Describe the morphology of the erythrocytes.
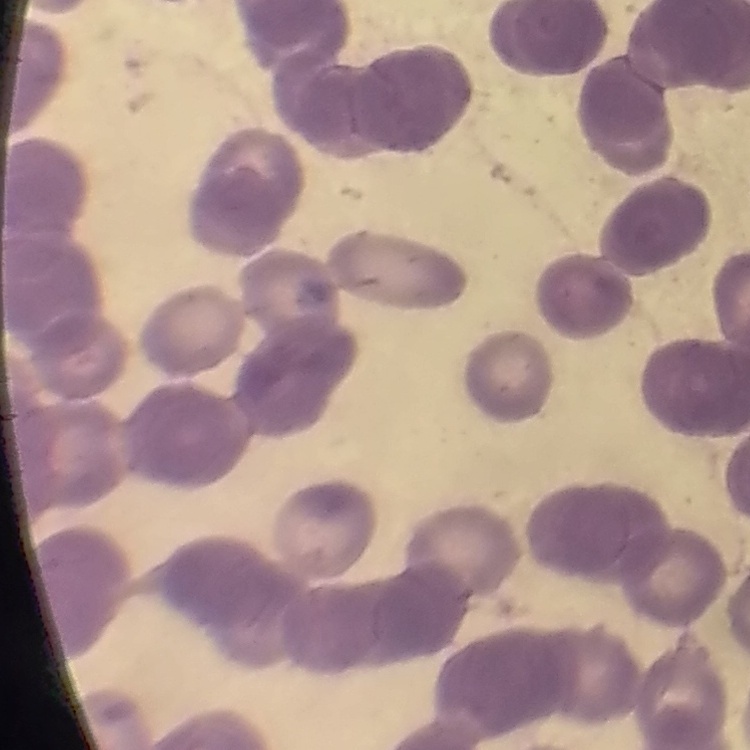
They show rouleaux formation.

preparation = thin blood film
image type = square crop of a larger photomicrograph
stain = Field's or Giemsa